Locate every malaria parasite and every leukocyte.
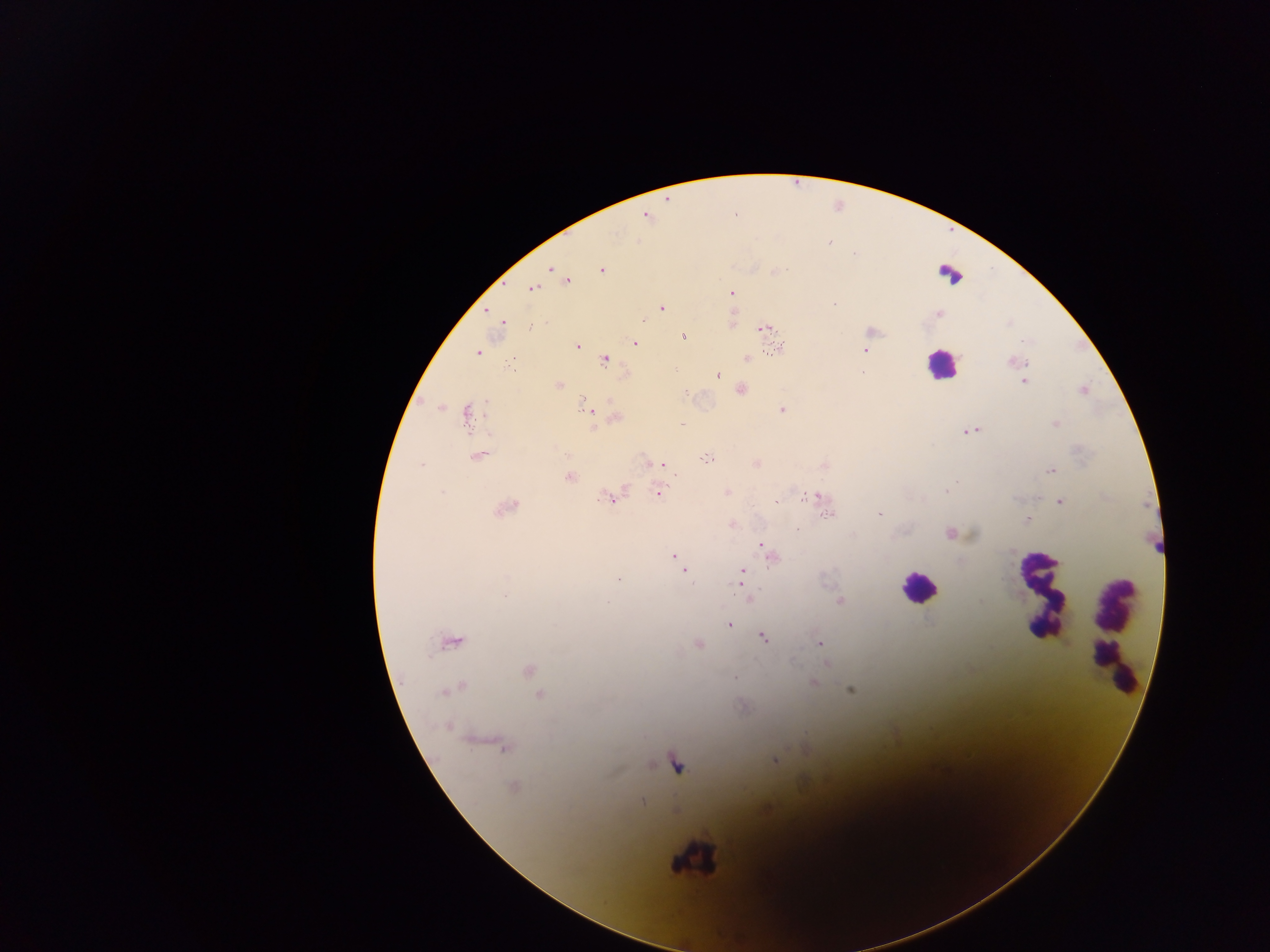

Approximate centers as {x, y} in pixels.
Malaria parasites: {646, 215}, {550, 269}, {601, 269}, {566, 282}, {532, 288}, {730, 293}, {834, 304}, {661, 307}, {489, 311}, {937, 313}, {731, 318}, {502, 321}, {763, 328}, {769, 329}, {871, 332}, {683, 336}, {634, 343}, {576, 345}, {779, 348}, {866, 349}, {477, 352}, {604, 359}, {747, 359}, {513, 360}, {1015, 361}, {716, 375}, {1024, 381}, {558, 385}, {741, 389}, {1082, 390}, {782, 409}, {588, 410}, {468, 414}, {615, 417}, {1055, 423}, {967, 431}, {478, 454}, {708, 457}, {650, 464}, {659, 464}, {756, 464}, {823, 464}, {1051, 470}, {568, 477}, {727, 492}, {658, 493}, {612, 497}, {816, 497}, {1059, 502}, {505, 507}, {828, 512}, {880, 514}, {1027, 519}, {732, 523}, {949, 532}, {762, 545}, {673, 556}, {771, 556}, {678, 562}, {685, 569}, {741, 572}, {749, 599}, {839, 601}, {730, 624}, {763, 637}, {451, 641}, {820, 643}, {698, 644}, {827, 664}, {528, 671}, {734, 677}, {812, 682}, {451, 688}, {851, 689}, {539, 693}, {503, 746}, {805, 748}, {774, 760}, {512, 787}, {642, 801}.
Leukocytes: {950, 275}, {941, 364}, {919, 588}, {1041, 595}, {1114, 633}, {1113, 640}, {678, 764}, {694, 858}.

Summary:
  - Capture: mobile-phone photograph through a microscope
  - Country: Ghana
  - Image size: 1270×952 pixels
  - Field of view: single
  - Preparation: thick blood smear